Classify this cell by malaria status.
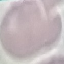

Uninfected.

Summary:
  - Stain: Giemsa
  - Image type: cell patch, automatically extracted from a larger field of view and resized to 64 × 64 pixels
  - Preparation: thin blood film
  - Capture: smartphone through the microscope eyepiece